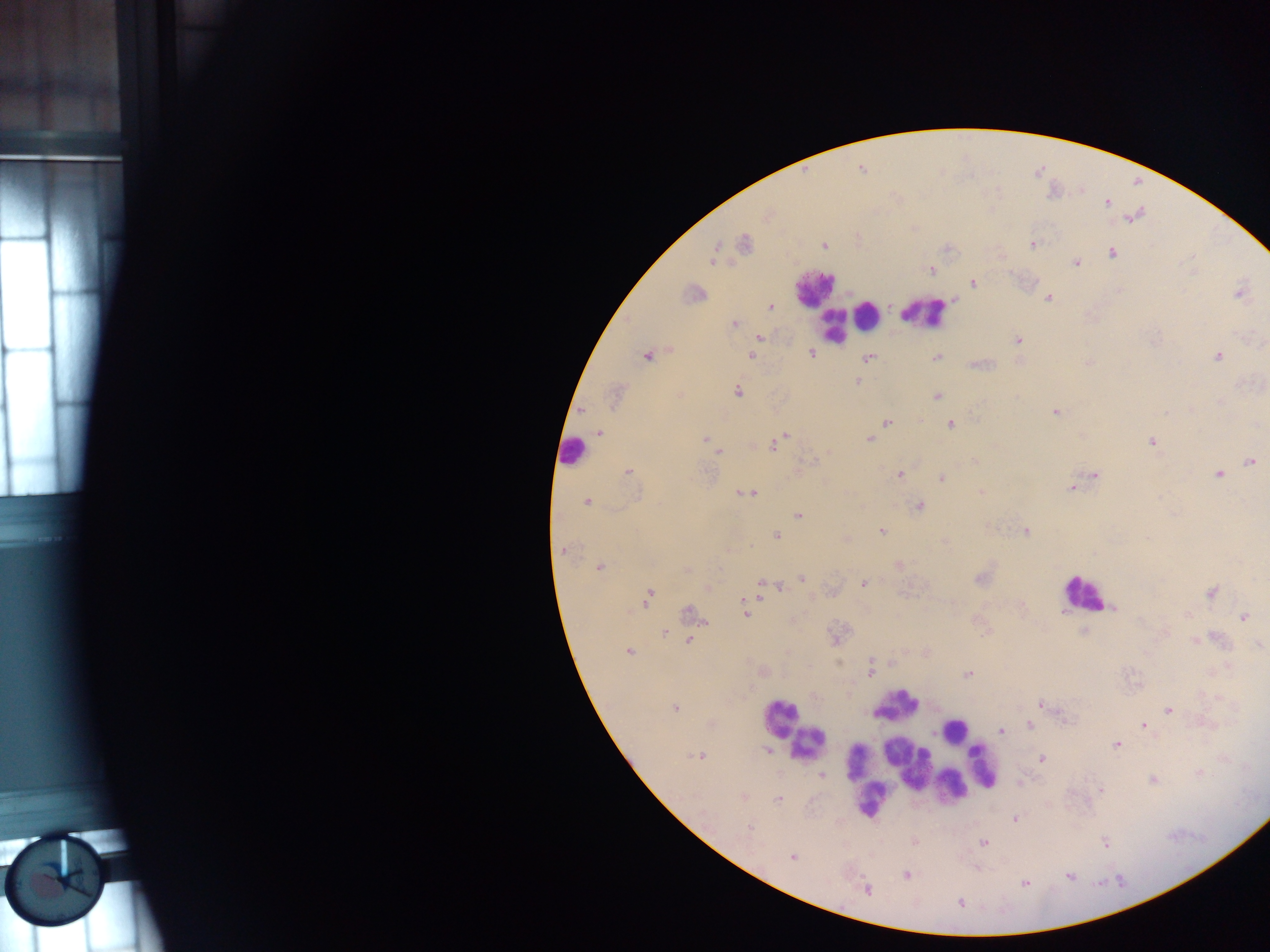

capture = mobile-phone photograph through a microscope
country = Ghana
malaria parasite locations = approximate centers as {x, y} in pixels: {861, 169}, {1108, 202}, {767, 216}, {744, 243}, {1033, 244}, {823, 246}, {1112, 253}, {713, 258}, {1077, 263}, {931, 271}, {973, 283}, {693, 293}, {1238, 294}, {1048, 298}, {770, 307}, {733, 324}, {760, 337}, {1017, 340}, {812, 353}, {647, 356}, {1218, 356}, {751, 357}, {937, 357}, {869, 358}, {858, 382}, {737, 391}, {615, 396}, {937, 396}, {1219, 402}, {1056, 412}, {887, 422}, {950, 425}, {600, 432}, {782, 438}, {869, 439}, {706, 440}, {1151, 442}, {774, 445}, {713, 449}, {718, 451}, {974, 460}, {1251, 461}, {806, 463}, {629, 471}, {900, 475}, {1094, 475}, {1218, 475}, {941, 478}, {1073, 488}, {746, 493}, {980, 493}, {587, 502}, {919, 506}, {798, 515}, {882, 531}, {1025, 531}, {776, 536}, {945, 541}, {564, 549}, {898, 564}, {599, 568}, {686, 571}, {802, 578}, {979, 579}, {864, 583}, {761, 585}, {708, 588}, {780, 588}, {763, 590}, {1212, 592}, {649, 596}, {1113, 608}, {690, 612}, {745, 612}, {1244, 617}, {664, 634}, {1216, 639}, {689, 640}, {1195, 641}, {1259, 645}, {628, 651}, {870, 668}, {968, 674}, {1041, 705}, {675, 707}, {1169, 710}, {1029, 724}, {1144, 726}, {1001, 731}, {1116, 745}, {767, 750}, {699, 756}, {1042, 759}, {1199, 773}, {822, 776}, {1153, 779}, {1101, 790}, {743, 797}, {778, 799}, {1015, 819}, {748, 826}, {983, 842}, {1105, 843}, {792, 857}, {907, 875}, {1068, 876}, {1025, 883}, {867, 890}, {960, 903}
preparation = thick blood smear
leukocyte locations = approximate centers as {x, y} in pixels: {813, 288}, {822, 300}, {926, 313}, {868, 314}, {832, 326}, {572, 451}, {1082, 593}, {899, 705}, {779, 717}, {952, 729}, {809, 743}, {859, 762}, {907, 763}, {984, 767}, {952, 786}, {869, 800}
field of view = single
image size = 1270×952 pixels